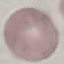
Summary:
  - Result: no malaria parasites detected
  - Capture: smartphone camera at the microscope eyepiece
  - Preparation: thin smear
  - Image type: cell patch, automatically extracted from a larger field of view and resized to 64 × 64 pixels
  - Stain: Giemsa